Name the cell type shown.
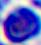

A leukocyte.

Summary:
  - Magnification: 400x
  - Modality: photomicrograph